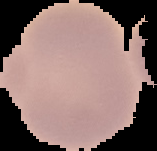

Summary:
  - Preparation: thin blood smear
  - Malaria status: uninfected
  - Image type: segmented cell region with the area outside set to black
  - Image size: 157×151 pixels